Outline each Plasmodium vivax-infected red blood cell.
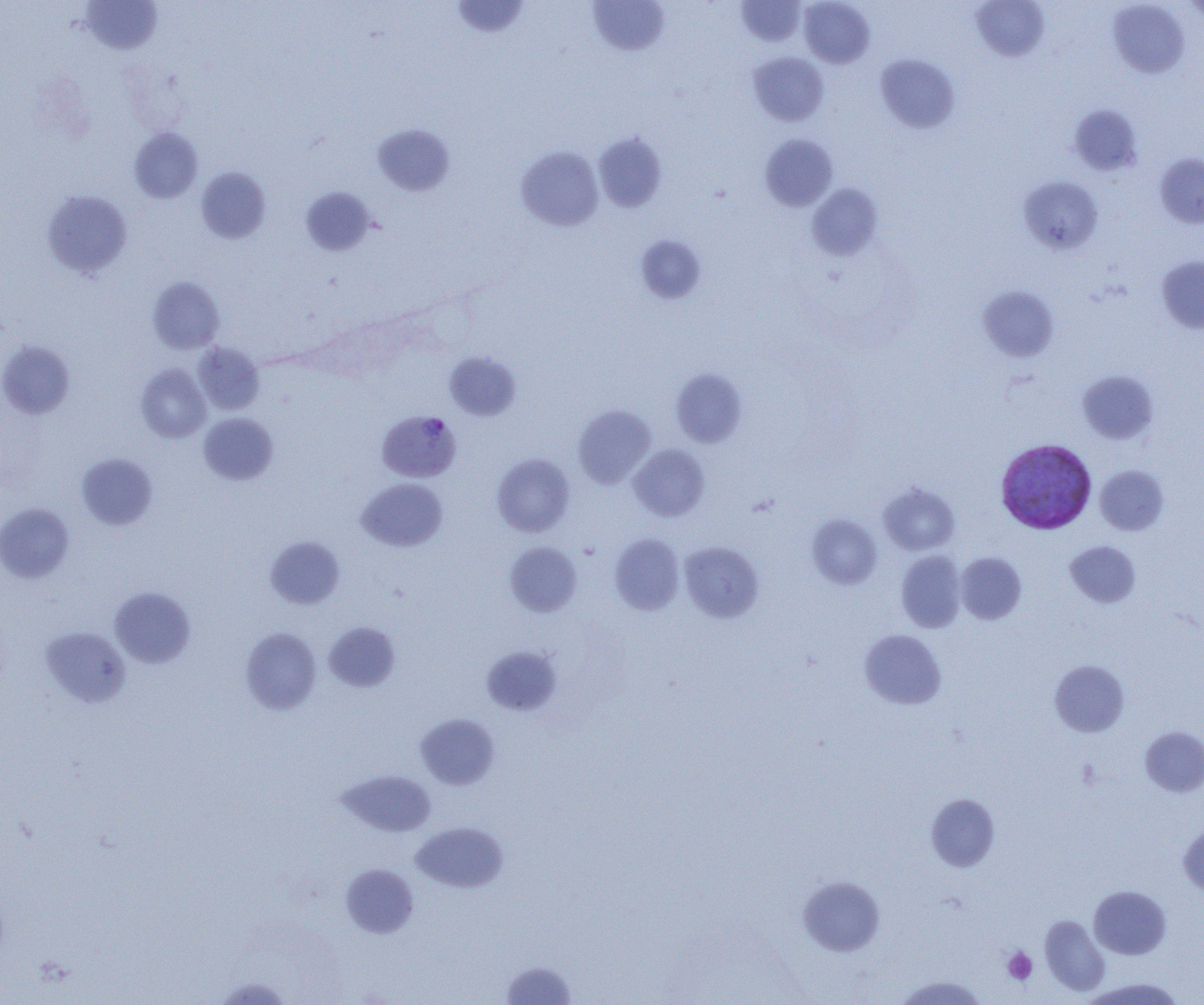
Approximate bounding boxes as [x1, y1, x2, y2] in pixels.
Plasmodium vivax-infected red blood cells: [377, 410, 462, 483], [995, 438, 1097, 534].

Summary:
  - Platelet locations: [1077, 760, 1101, 789], [1002, 947, 1038, 985]
  - Uninfected red blood cell locations: [450, 0, 530, 39], [735, 0, 807, 47], [799, 0, 875, 68], [971, 0, 1050, 61], [80, 1, 163, 55], [587, 1, 670, 56], [1108, 1, 1191, 78], [1182, 1, 1204, 22], [748, 51, 829, 126], [875, 53, 960, 133], [1068, 104, 1144, 175], [372, 124, 455, 196], [129, 128, 203, 203], [593, 131, 668, 213], [759, 134, 838, 211], [516, 146, 604, 231], [1155, 153, 1204, 228], [196, 167, 271, 243], [1019, 176, 1103, 255], [806, 183, 883, 261], [301, 187, 375, 256], [42, 190, 132, 278], [635, 234, 707, 304], [1156, 255, 1204, 334], [147, 276, 224, 354], [978, 285, 1059, 362], [0, 341, 75, 419], [194, 342, 264, 415], [444, 351, 522, 421], [136, 363, 211, 443], [670, 368, 748, 448], [1078, 370, 1158, 444], [572, 404, 656, 489], [199, 413, 277, 485], [628, 443, 710, 521], [76, 453, 158, 530], [491, 453, 575, 537], [1095, 465, 1169, 535], [357, 478, 448, 552], [878, 482, 960, 555], [0, 502, 75, 582], [807, 514, 882, 589], [609, 533, 685, 615], [265, 536, 345, 609], [1065, 540, 1141, 608], [679, 541, 763, 623], [504, 542, 582, 617], [896, 551, 967, 632], [956, 552, 1027, 624], [109, 587, 196, 668], [323, 621, 401, 692], [40, 626, 131, 708], [240, 627, 322, 714], [859, 629, 946, 709], [481, 645, 562, 716], [1049, 660, 1130, 737], [415, 713, 500, 790], [1140, 726, 1204, 797], [338, 770, 437, 836], [926, 793, 1000, 872], [411, 821, 508, 893], [1178, 824, 1204, 897], [340, 864, 419, 938], [797, 875, 885, 956], [1089, 885, 1171, 959], [1039, 915, 1109, 995], [501, 959, 577, 1004], [895, 975, 988, 1005], [212, 976, 295, 1005], [1082, 978, 1184, 1004]
  - Slide-level diagnosis: Plasmodium vivax
  - Magnification: 1000x
  - Modality: optical microscopy
  - Field of view: single
  - Preparation: thin blood film
  - Image size: 1204×1005 pixels